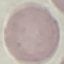 Malaria status: uninfected. Cell patch, automatically extracted from a larger field of view and resized to 64 × 64 pixels. Giemsa-stained preparation. Thin blood film. Acquired by smartphone through the microscope eyepiece.